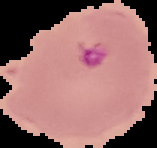
Summary:
  - Image type: segmented cell region with the area outside set to black
  - Image size: 157×148 pixels
  - Malaria status: parasitized
  - Preparation: thin blood smear